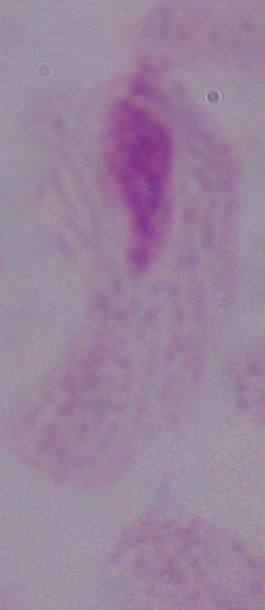

Summary:
  - Identification: trichomonad
  - Magnification: 1000x
  - Modality: photomicrograph